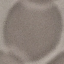

Result: no malaria parasites seen. Giemsa stain. Acquired by smartphone through the microscope eyepiece. Automatically extracted cell patch, resized to 64 × 64 pixels. Thin blood smear.